Assess this cell for malaria.
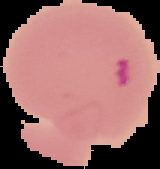
Parasitized.

Image is 160×169 pixels. From a thin blood smear. Cell region segmented out of the field of view; the surrounding area is masked to black.